Locate every blood parasite and identify its species.
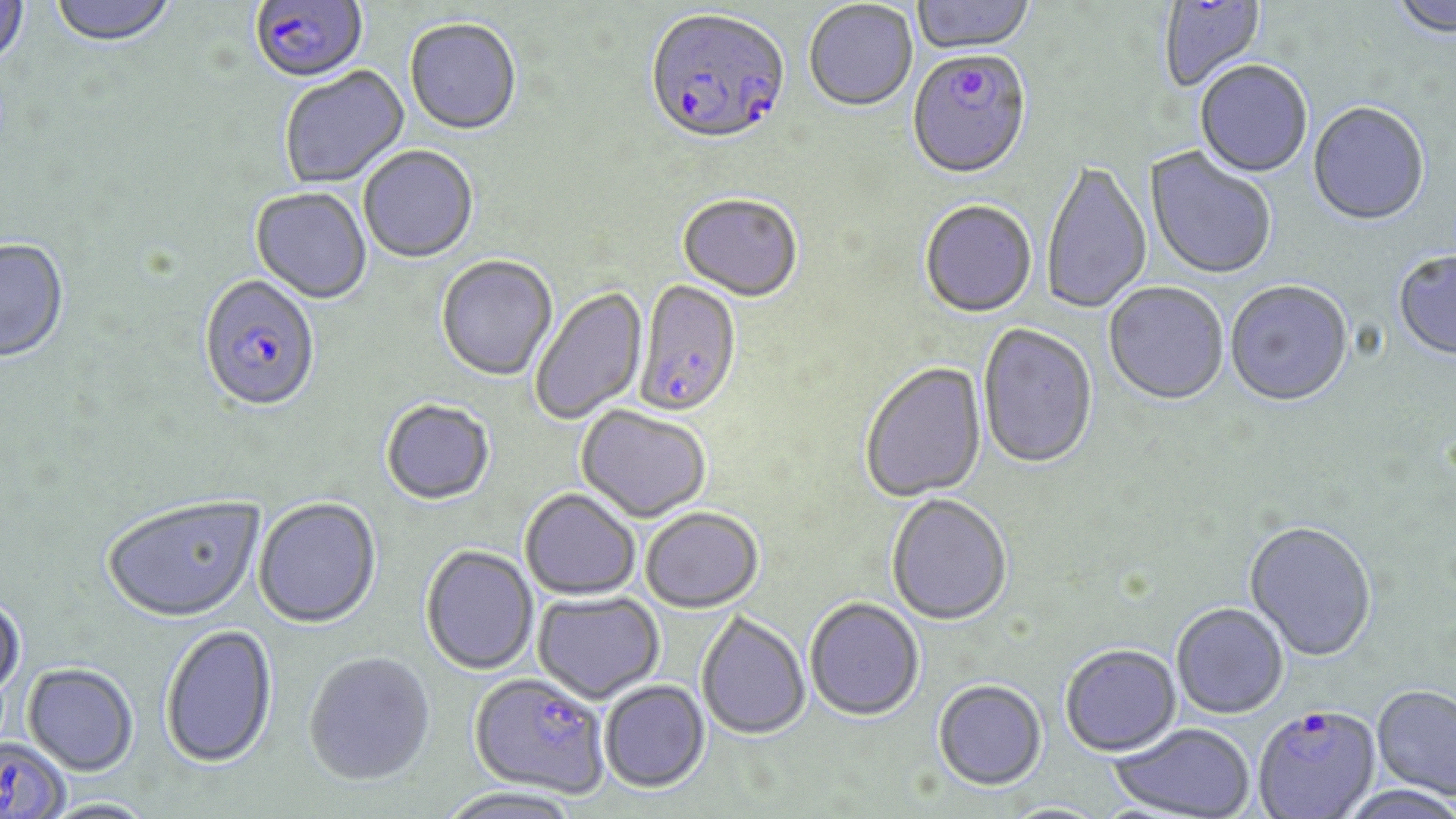
Approximate bounding boxes as (x1, y1, x2, y2) in pixels.
Plasmodium falciparum-infected red blood cells: (250, 0, 369, 85), (643, 10, 790, 150), (906, 53, 1031, 182), (198, 276, 321, 415), (634, 281, 741, 419), (468, 673, 609, 798), (1253, 705, 1380, 819), (0, 737, 72, 819).
No Plasmodium ovale, Plasmodium malariae, Plasmodium vivax, Babesia divergens, or Trypanosoma brucei observed.

Summary:
  - Uninfected red blood cell locations: (49, 0, 179, 49), (912, 0, 1036, 57), (1160, 0, 1268, 94), (1389, 0, 1455, 42), (0, 1, 29, 71), (804, 2, 918, 114), (405, 20, 521, 137), (1195, 62, 1312, 179), (279, 67, 411, 189), (1308, 104, 1430, 229), (359, 147, 479, 265), (1144, 148, 1277, 282), (1041, 161, 1152, 316), (250, 188, 372, 305), (678, 196, 802, 303), (919, 201, 1037, 320), (0, 239, 70, 365), (1393, 252, 1456, 362), (436, 256, 558, 382), (1225, 282, 1353, 409), (1103, 283, 1229, 407), (530, 286, 649, 424), (977, 325, 1098, 472), (860, 363, 987, 504), (380, 399, 495, 505), (575, 406, 712, 524), (519, 489, 640, 600), (102, 494, 265, 622), (887, 496, 1012, 627), (253, 497, 382, 629), (640, 508, 763, 613), (1244, 521, 1377, 663), (420, 545, 539, 675), (533, 591, 664, 703), (0, 593, 25, 702), (805, 598, 924, 723), (1171, 603, 1288, 720), (697, 612, 811, 741), (160, 624, 278, 769), (1060, 644, 1181, 756), (302, 651, 436, 786), (23, 662, 138, 774), (599, 680, 711, 793), (932, 680, 1047, 791), (1371, 684, 1456, 800), (1108, 722, 1256, 818), (436, 787, 585, 819), (38, 798, 160, 818)
  - Slide-level diagnosis: Plasmodium falciparum
  - Field of view: one of a larger specimen
  - Stain: May-Grünwald-Giemsa
  - Magnification: 1000x
  - Modality: optical microscopy
  - Preparation: thin blood film
  - Image size: 1456×819 pixels